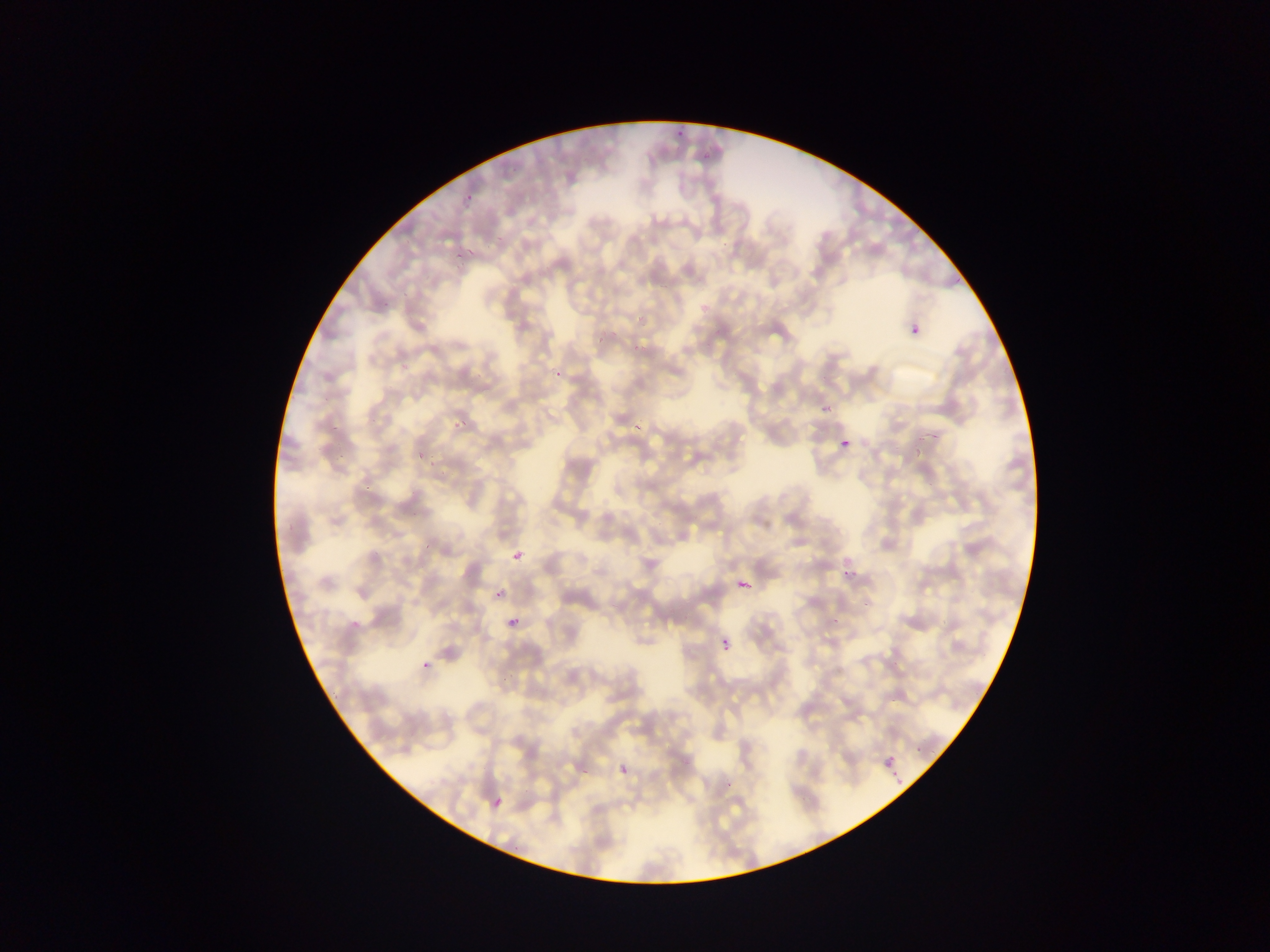
Approximate bounding boxes as [left, top, right, bottom] in pixels.
Summary:
  - Malaria parasite locations: [674, 126, 687, 135], [696, 151, 710, 165], [463, 193, 473, 200], [493, 237, 503, 244], [465, 245, 477, 254], [453, 254, 462, 263], [378, 299, 388, 313], [906, 318, 927, 344], [593, 334, 604, 343], [630, 335, 651, 350], [388, 354, 416, 370], [548, 370, 562, 379], [816, 404, 829, 414], [448, 417, 475, 431], [329, 419, 342, 437], [637, 420, 640, 432], [835, 434, 857, 457], [331, 444, 352, 459], [415, 447, 424, 459], [426, 459, 439, 472], [362, 480, 379, 492], [419, 541, 431, 552], [510, 549, 526, 566], [837, 569, 854, 582], [733, 574, 756, 598], [490, 593, 502, 601], [856, 596, 871, 610], [831, 609, 845, 629], [348, 611, 362, 629], [506, 614, 524, 631], [717, 633, 737, 655], [417, 658, 431, 675], [879, 754, 904, 783], [579, 763, 592, 775], [620, 764, 631, 777], [491, 793, 510, 814]
  - Country: Ghana
  - Field of view: single
  - Preparation: thin blood film
  - Capture: mobile-phone photograph through a microscope
  - Image size: 1270×952 pixels